Outline each uninfected red blood cell.
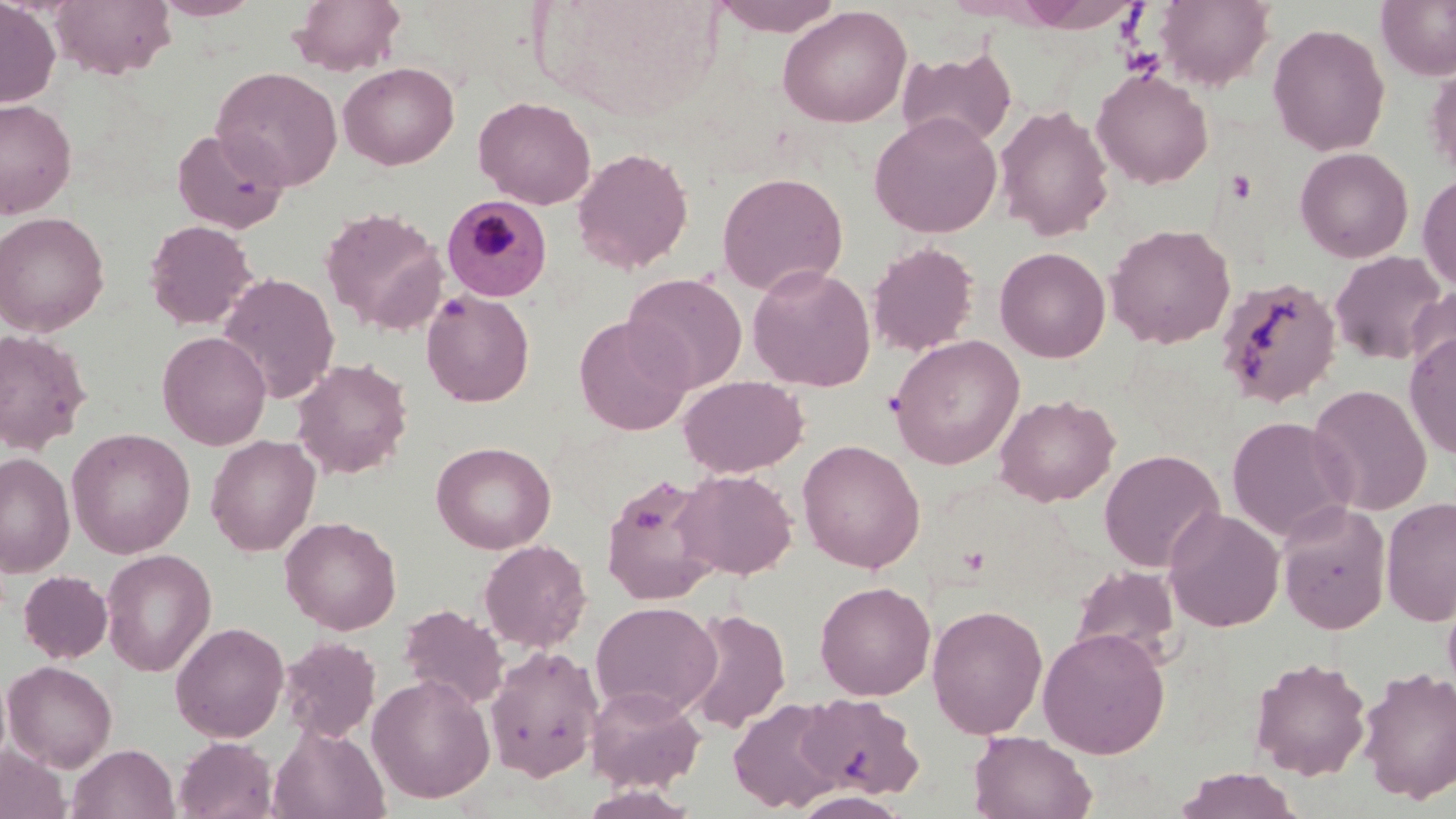

Approximate bounding boxes as named x1/y1/x2/y2 corners in pixels.
Uninfected red blood cells: (x1=0, y1=0, x2=61, y2=108), (x1=50, y1=0, x2=176, y2=79), (x1=152, y1=0, x2=263, y2=21), (x1=289, y1=0, x2=406, y2=77), (x1=709, y1=0, x2=845, y2=37), (x1=1154, y1=0, x2=1275, y2=90), (x1=1376, y1=0, x2=1456, y2=80), (x1=777, y1=5, x2=912, y2=128), (x1=1267, y1=22, x2=1391, y2=157), (x1=896, y1=45, x2=1018, y2=152), (x1=1425, y1=60, x2=1456, y2=181), (x1=338, y1=61, x2=459, y2=170), (x1=211, y1=66, x2=343, y2=191), (x1=1091, y1=67, x2=1214, y2=189), (x1=473, y1=96, x2=596, y2=209), (x1=0, y1=97, x2=77, y2=218), (x1=994, y1=103, x2=1114, y2=242), (x1=868, y1=111, x2=1003, y2=238), (x1=171, y1=127, x2=289, y2=234), (x1=571, y1=147, x2=694, y2=274), (x1=1294, y1=147, x2=1414, y2=263), (x1=716, y1=171, x2=849, y2=297), (x1=1417, y1=173, x2=1456, y2=292), (x1=320, y1=206, x2=448, y2=335), (x1=0, y1=211, x2=110, y2=336), (x1=144, y1=219, x2=258, y2=330), (x1=1104, y1=223, x2=1236, y2=349), (x1=867, y1=242, x2=980, y2=357), (x1=994, y1=246, x2=1111, y2=363), (x1=1329, y1=250, x2=1449, y2=366), (x1=747, y1=264, x2=876, y2=392), (x1=218, y1=273, x2=340, y2=403), (x1=623, y1=273, x2=748, y2=393), (x1=1213, y1=275, x2=1343, y2=409), (x1=1406, y1=285, x2=1456, y2=385), (x1=421, y1=289, x2=535, y2=407), (x1=574, y1=315, x2=692, y2=436), (x1=0, y1=329, x2=92, y2=454), (x1=157, y1=331, x2=272, y2=450), (x1=1404, y1=331, x2=1456, y2=459), (x1=888, y1=334, x2=1025, y2=470), (x1=291, y1=357, x2=413, y2=479), (x1=678, y1=375, x2=809, y2=477), (x1=1307, y1=384, x2=1432, y2=516), (x1=994, y1=393, x2=1120, y2=507), (x1=1226, y1=416, x2=1356, y2=542), (x1=66, y1=427, x2=195, y2=558), (x1=205, y1=434, x2=321, y2=556), (x1=797, y1=439, x2=925, y2=573), (x1=431, y1=440, x2=556, y2=554), (x1=1099, y1=448, x2=1225, y2=572), (x1=1, y1=452, x2=75, y2=577), (x1=674, y1=468, x2=798, y2=580), (x1=601, y1=474, x2=722, y2=606), (x1=1381, y1=495, x2=1456, y2=626), (x1=1276, y1=502, x2=1392, y2=633), (x1=1163, y1=506, x2=1285, y2=632), (x1=279, y1=516, x2=401, y2=635), (x1=479, y1=539, x2=592, y2=652), (x1=101, y1=549, x2=216, y2=676), (x1=1070, y1=563, x2=1182, y2=667), (x1=18, y1=570, x2=113, y2=663), (x1=815, y1=580, x2=936, y2=700), (x1=1442, y1=588, x2=1456, y2=701), (x1=590, y1=600, x2=722, y2=719), (x1=927, y1=603, x2=1048, y2=739), (x1=399, y1=604, x2=509, y2=709), (x1=681, y1=606, x2=791, y2=733), (x1=171, y1=622, x2=289, y2=742), (x1=1037, y1=627, x2=1170, y2=759), (x1=279, y1=635, x2=381, y2=742), (x1=485, y1=645, x2=603, y2=781), (x1=1249, y1=656, x2=1371, y2=780), (x1=2, y1=660, x2=118, y2=772), (x1=1356, y1=666, x2=1456, y2=804), (x1=367, y1=673, x2=495, y2=803), (x1=585, y1=684, x2=706, y2=792), (x1=796, y1=693, x2=924, y2=799), (x1=727, y1=698, x2=844, y2=813), (x1=270, y1=725, x2=390, y2=819), (x1=968, y1=730, x2=1097, y2=819), (x1=174, y1=736, x2=277, y2=819), (x1=68, y1=743, x2=179, y2=819), (x1=0, y1=745, x2=69, y2=819), (x1=1174, y1=767, x2=1304, y2=818), (x1=789, y1=791, x2=913, y2=819).

Plasmodium malariae-infected red blood cell locations: (x1=442, y1=195, x2=552, y2=302). Slide-level diagnosis: Plasmodium malariae. Captured at 1000x magnification. May-Grünwald-Giemsa stain. Image is 1456×819 pixels. Thin blood smear. Optical microscopy. One field of a larger specimen.